Locate every uninfected red blood cell.
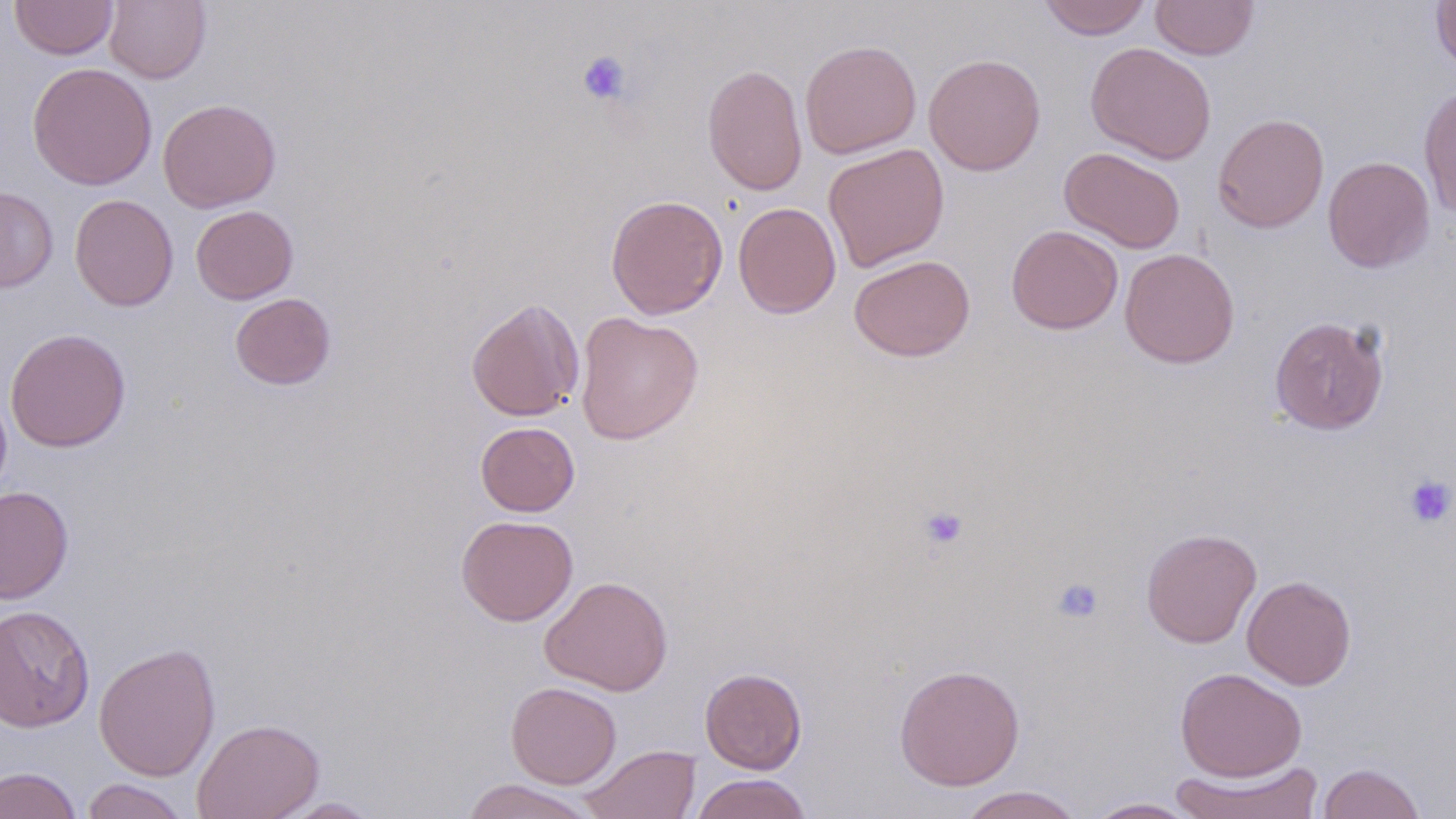
Approximate bounding boxes as (x1, y1, x2, y2) in pixels.
Uninfected red blood cells: (9, 0, 119, 60), (104, 0, 211, 84), (1037, 0, 1152, 40), (1151, 1, 1258, 60), (1431, 1, 1456, 75), (799, 40, 922, 159), (1085, 42, 1217, 164), (923, 53, 1046, 176), (27, 63, 158, 190), (702, 63, 807, 196), (1418, 84, 1456, 218), (157, 98, 281, 212), (1212, 113, 1330, 233), (823, 143, 950, 272), (1059, 147, 1186, 253), (1323, 156, 1435, 273), (0, 187, 58, 293), (69, 193, 178, 311), (605, 194, 728, 320), (733, 202, 841, 319), (191, 204, 298, 304), (1006, 224, 1123, 334), (1119, 248, 1240, 368), (848, 254, 976, 362), (230, 293, 336, 390), (465, 297, 584, 422), (574, 311, 704, 444), (1269, 315, 1390, 435), (4, 328, 131, 452), (0, 384, 13, 507), (475, 422, 580, 516), (0, 486, 74, 604), (456, 514, 578, 626), (1140, 527, 1262, 649), (539, 575, 673, 696), (1242, 575, 1357, 690), (0, 604, 96, 731), (93, 642, 221, 782), (894, 664, 1025, 790), (700, 667, 807, 774), (1175, 667, 1306, 781), (505, 681, 622, 789), (192, 717, 325, 819), (579, 744, 701, 819), (1168, 759, 1325, 819), (1317, 763, 1426, 819), (1, 765, 83, 819), (690, 773, 813, 819), (80, 778, 191, 819), (460, 779, 600, 819), (955, 785, 1086, 819), (272, 797, 385, 818), (1083, 797, 1204, 818).

Summary:
  - Platelet locations: (576, 50, 631, 106), (1404, 474, 1455, 527), (919, 505, 969, 551), (1050, 576, 1104, 625)
  - Slide-level diagnosis: negative for blood parasites
  - Stain: May-Grünwald-Giemsa
  - Preparation: thin blood smear
  - Magnification: 1000x
  - Image size: 1456×819 pixels
  - Field of view: single
  - Modality: light microscopy